Locate every blood parasite and identify its species.
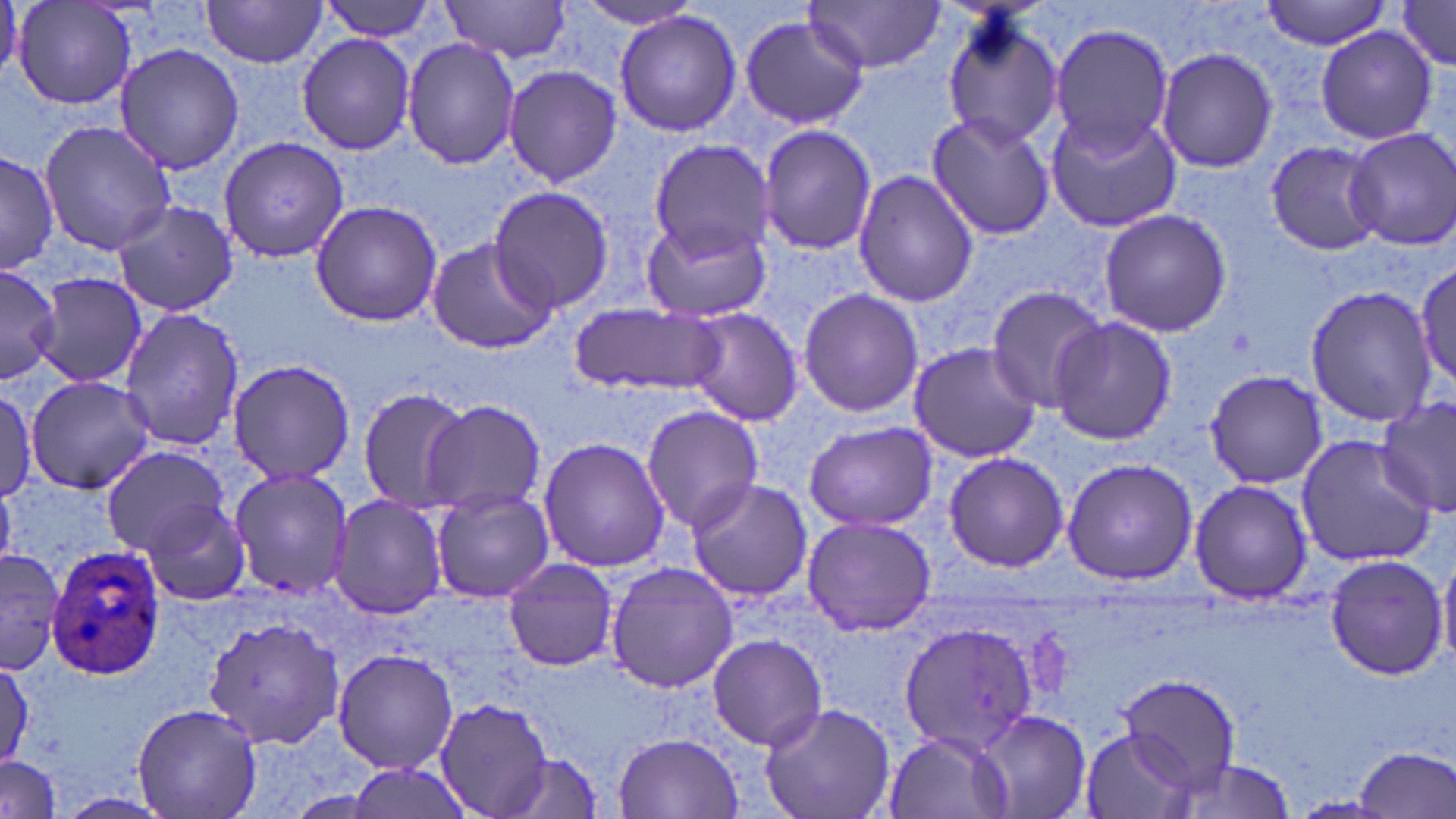

Approximate bounding boxes as [x1, y1, x2, y2] in pixels.
Plasmodium ovale-infected red blood cells: [45, 543, 168, 683].
No Plasmodium falciparum, Plasmodium malariae, Plasmodium vivax, Babesia divergens, or Trypanosoma brucei observed.

slide_level_diagnosis: Plasmodium ovale
image_size: 1456×819 pixels
stain: May-Grünwald-Giemsa
preparation: thin blood film
magnification: 1000x
field_of_view: single
modality: optical microscopy
uninfected_red_blood_cell_locations: 'approximate bounding boxes as [x1, y1, x2, y2] in pixels: [12, 0, 136, 112], [319, 0, 442, 41], [439, 0, 573, 64], [566, 0, 710, 30], [1261, 1, 1394, 51], [199, 2, 330, 67], [803, 2, 947, 74], [1391, 2, 1456, 71], [939, 8, 1063, 152], [613, 10, 742, 138], [739, 14, 868, 130], [1049, 25, 1173, 153], [1316, 27, 1437, 145], [297, 33, 415, 155], [402, 38, 520, 169], [113, 43, 244, 175], [1155, 47, 1279, 174], [503, 65, 623, 189], [1047, 109, 1181, 233], [925, 112, 1056, 240], [37, 120, 175, 255], [758, 125, 877, 256], [1341, 126, 1456, 250], [218, 136, 349, 264], [647, 140, 772, 260], [1264, 140, 1390, 256], [0, 148, 60, 277], [852, 170, 979, 307], [486, 188, 616, 314], [110, 198, 238, 319], [309, 201, 443, 327], [1098, 208, 1232, 337], [640, 216, 770, 322], [423, 238, 557, 354], [1414, 261, 1455, 389], [0, 264, 61, 386], [36, 274, 156, 389], [1305, 284, 1436, 429], [983, 286, 1106, 410], [797, 287, 923, 418], [569, 303, 721, 395], [117, 306, 244, 451], [684, 307, 805, 427], [1048, 315, 1176, 447], [906, 341, 1042, 462], [226, 357, 356, 485], [1203, 368, 1326, 490], [25, 376, 155, 495], [354, 387, 473, 514], [0, 388, 38, 501], [1374, 397, 1454, 515], [422, 400, 546, 516], [642, 405, 766, 534], [804, 420, 938, 530], [1296, 433, 1439, 565], [537, 437, 670, 574], [101, 446, 229, 555], [942, 450, 1068, 572], [1061, 457, 1198, 586], [227, 465, 354, 601], [683, 477, 813, 604], [1189, 479, 1314, 605], [431, 488, 554, 603], [329, 493, 446, 620], [136, 498, 251, 605], [802, 515, 935, 637], [0, 542, 69, 677], [1321, 553, 1450, 679], [1438, 555, 1456, 669], [502, 558, 619, 672], [605, 562, 737, 694], [202, 614, 345, 753], [897, 620, 1039, 757], [707, 633, 827, 750], [331, 648, 459, 774], [0, 656, 34, 769], [1116, 673, 1241, 787], [433, 697, 553, 817], [758, 701, 896, 819], [130, 702, 264, 818], [974, 708, 1091, 818], [1077, 726, 1196, 819], [883, 728, 1019, 819], [612, 732, 744, 818], [1352, 746, 1456, 819], [501, 754, 605, 819], [0, 755, 61, 819], [1164, 757, 1298, 818]'